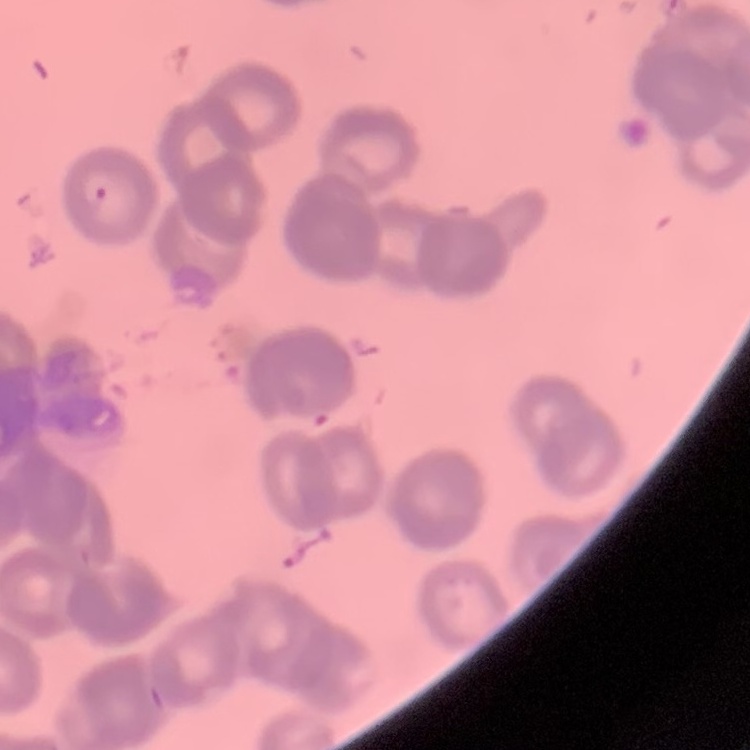

erythrocyte morphology = rouleaux formation
image type = one tile cut from a larger photomicrograph
stain = Field's or Giemsa
preparation = thin blood film